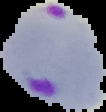

From a thin blood smear. Segmented cell region on a black background. Malaria status: parasitized. Image is 106×112 pixels.